Assess this cell for malaria.
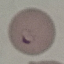
Parasitized.

Automatically extracted cell patch, resized to 64 × 64 pixels. Acquired by smartphone through the microscope eyepiece. Thin blood film. Giemsa stain.